Identify the cell.
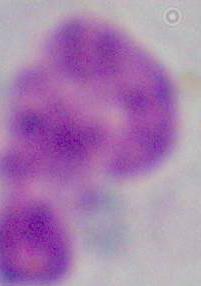

This is a leukocyte.

{
  "magnification": "1000x",
  "modality": "micrograph"
}